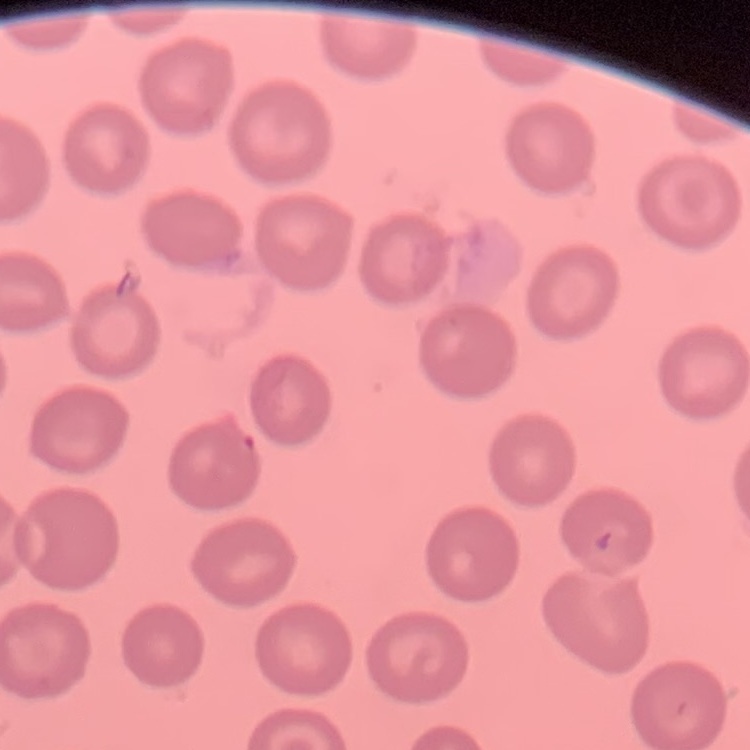
{
  "erythrocyte_morphology": "no rouleaux formation",
  "image_type": "one tile cut from a larger photomicrograph",
  "preparation": "thin blood smear",
  "stain": "Field's or Giemsa"
}